Name the blood parasite species.
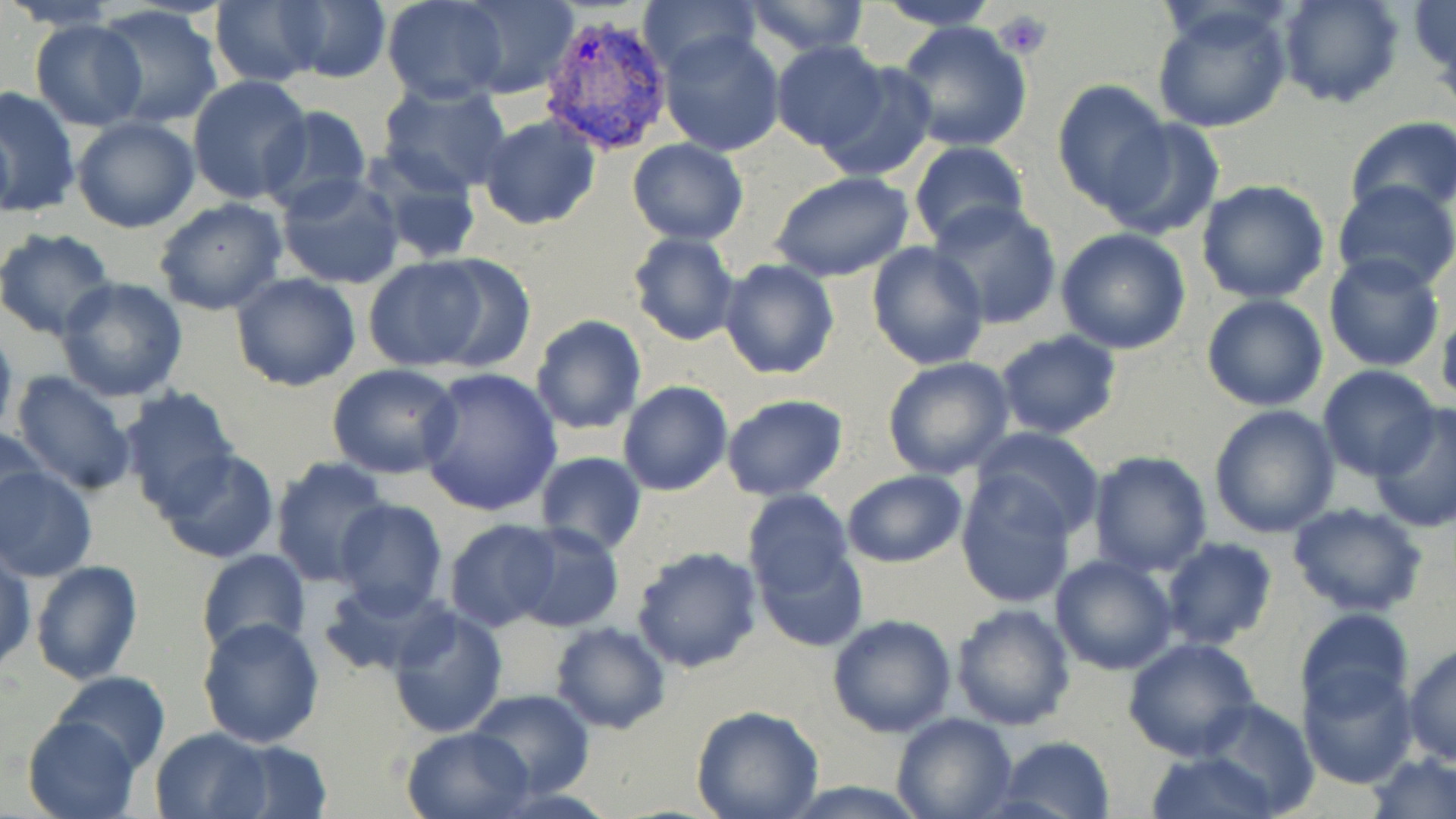

Plasmodium vivax.

Approximate bounding boxes as (x1, y1, x2, y2) in pixels. Platelet locations: (995, 9, 1051, 60). Uninfected red blood cell locations: (9, 0, 125, 29), (278, 0, 392, 85), (383, 0, 510, 104), (460, 0, 577, 98), (639, 0, 761, 78), (741, 0, 872, 57), (871, 0, 1003, 31), (1275, 0, 1403, 109), (209, 2, 326, 86), (1149, 2, 1295, 135), (94, 5, 223, 129), (895, 20, 1032, 152), (29, 21, 147, 129), (657, 29, 786, 157), (771, 41, 889, 154), (815, 61, 937, 184), (187, 77, 312, 206), (1052, 80, 1174, 212), (377, 82, 514, 197), (0, 86, 80, 218), (72, 99, 308, 220), (258, 106, 373, 216), (478, 114, 600, 230), (71, 116, 201, 234), (1347, 116, 1456, 219), (1102, 117, 1225, 241), (626, 138, 748, 244), (907, 140, 1030, 247), (363, 148, 481, 264), (768, 171, 915, 283), (276, 174, 406, 292), (1195, 179, 1329, 303), (1331, 180, 1456, 294), (154, 198, 287, 316), (928, 201, 1062, 327), (0, 228, 116, 341), (1055, 229, 1192, 355), (627, 231, 740, 346), (866, 241, 990, 369), (1323, 252, 1446, 372), (414, 253, 538, 374), (363, 257, 493, 371), (717, 258, 840, 380), (229, 271, 362, 392), (55, 275, 189, 403), (1201, 294, 1328, 411), (1438, 303, 1456, 409), (531, 315, 648, 436), (0, 324, 18, 444), (994, 330, 1124, 440), (882, 357, 1016, 479), (328, 364, 464, 480), (417, 366, 563, 517), (1317, 366, 1441, 481), (9, 370, 139, 496), (618, 382, 733, 496), (115, 386, 243, 516), (721, 393, 850, 500), (1370, 403, 1456, 531), (1208, 405, 1341, 539), (1, 424, 48, 531), (973, 426, 1107, 537), (157, 448, 280, 565), (1086, 450, 1215, 575), (535, 453, 646, 555), (269, 456, 388, 587), (0, 464, 96, 582), (841, 470, 967, 567), (955, 472, 1077, 608), (743, 490, 855, 601), (332, 499, 448, 618), (1285, 502, 1431, 619), (444, 520, 562, 633), (506, 523, 625, 632), (1159, 536, 1278, 649), (752, 540, 867, 652), (632, 545, 763, 671), (0, 548, 35, 675), (195, 549, 310, 661), (1050, 555, 1179, 675), (29, 559, 144, 684), (320, 578, 448, 677), (949, 602, 1076, 732), (386, 604, 508, 738), (1295, 608, 1414, 719), (828, 613, 958, 737), (197, 616, 325, 748), (549, 621, 671, 733), (1122, 635, 1259, 762), (1403, 643, 1456, 765), (1297, 664, 1417, 787), (51, 670, 171, 773), (466, 690, 593, 799), (1197, 698, 1319, 814), (691, 706, 824, 819), (891, 710, 1018, 819), (21, 713, 140, 819), (400, 724, 535, 818), (150, 728, 273, 818), (994, 737, 1116, 819), (217, 739, 333, 818), (1144, 751, 1281, 819), (1367, 751, 1456, 819), (776, 781, 934, 818). Plasmodium vivax-infected red blood cell locations: (540, 12, 674, 155). Image is 1456×819 pixels. Thin blood smear. Captured at 1000x magnification. One field of a larger specimen. May-Grünwald-Giemsa-stained preparation. Optical microscopy.